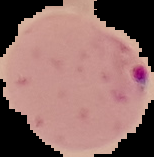
image size = 154×157 pixels
preparation = thin blood smear
result = malaria parasites detected
image type = segmented cell region with the area outside set to black